Give the position of every malaria parasite and every leukocyte.
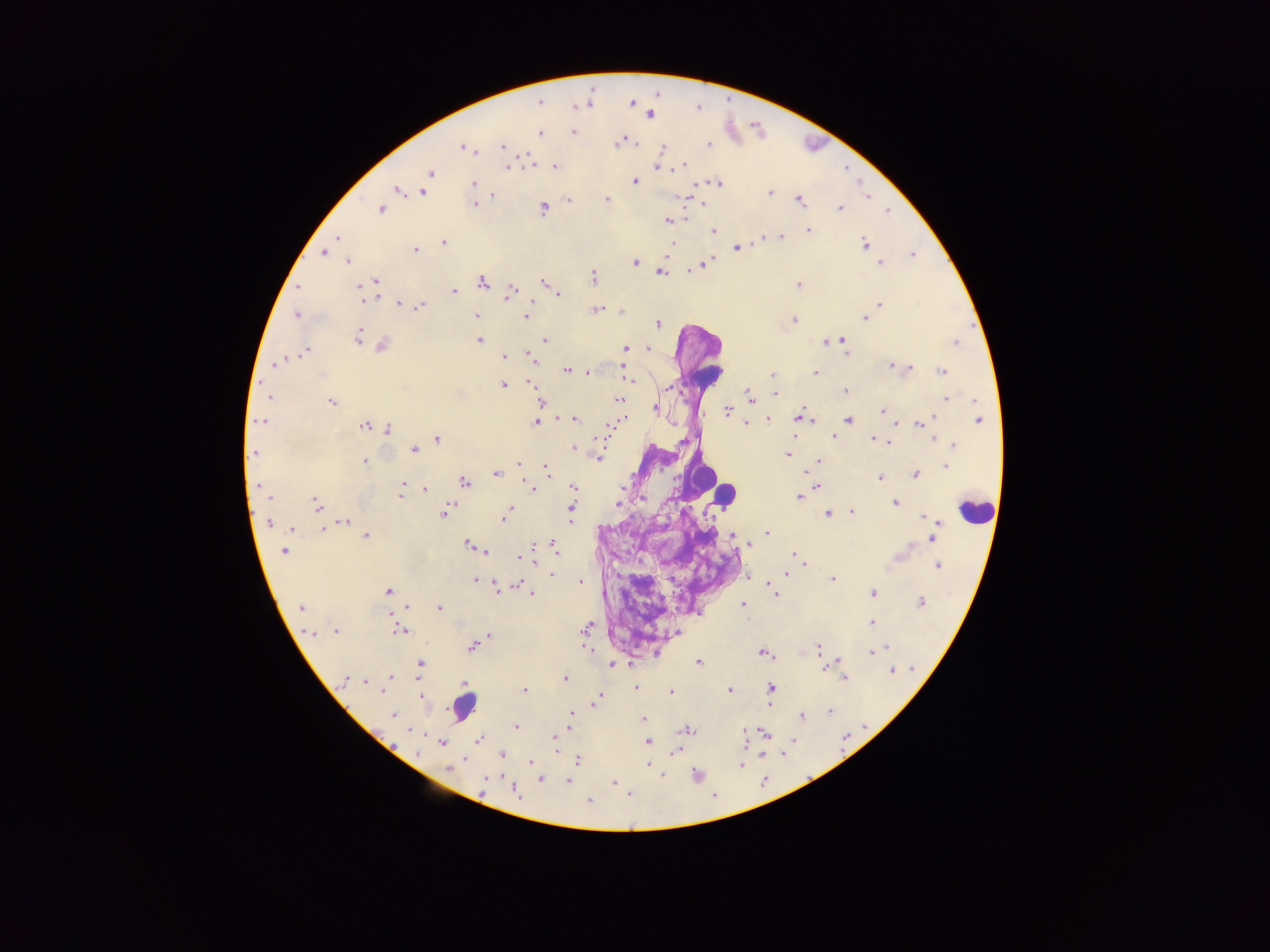

Approximate centers as {x, y} in pixels.
Malaria parasites: {540, 102}, {632, 103}, {589, 104}, {575, 105}, {650, 114}, {573, 132}, {539, 133}, {618, 142}, {503, 145}, {709, 145}, {464, 147}, {660, 148}, {528, 160}, {683, 164}, {507, 167}, {554, 167}, {659, 167}, {430, 173}, {635, 181}, {717, 182}, {473, 184}, {398, 189}, {423, 192}, {770, 193}, {491, 194}, {867, 196}, {681, 197}, {606, 199}, {799, 199}, {568, 201}, {702, 202}, {472, 203}, {542, 207}, {381, 208}, {840, 208}, {885, 211}, {668, 220}, {808, 231}, {713, 232}, {775, 236}, {781, 236}, {337, 238}, {762, 239}, {442, 242}, {865, 245}, {735, 248}, {414, 249}, {323, 253}, {912, 255}, {348, 260}, {635, 263}, {880, 263}, {703, 264}, {660, 271}, {592, 277}, {375, 281}, {482, 281}, {544, 283}, {798, 284}, {373, 285}, {298, 287}, {454, 291}, {509, 291}, {364, 292}, {376, 293}, {559, 295}, {532, 300}, {399, 303}, {879, 304}, {420, 306}, {597, 309}, {620, 311}, {297, 315}, {476, 315}, {526, 317}, {864, 318}, {793, 320}, {658, 324}, {358, 336}, {365, 340}, {479, 340}, {544, 340}, {841, 340}, {827, 342}, {956, 342}, {381, 345}, {625, 348}, {647, 348}, {304, 351}, {844, 351}, {528, 355}, {503, 356}, {278, 363}, {893, 365}, {903, 367}, {910, 368}, {567, 370}, {625, 370}, {587, 372}, {941, 372}, {815, 373}, {772, 375}, {531, 382}, {631, 382}, {503, 385}, {844, 391}, {775, 394}, {749, 396}, {268, 398}, {947, 399}, {618, 400}, {331, 402}, {540, 402}, {654, 409}, {726, 410}, {882, 411}, {799, 415}, {574, 418}, {767, 418}, {932, 418}, {979, 419}, {848, 420}, {812, 421}, {260, 422}, {535, 422}, {894, 423}, {917, 423}, {745, 424}, {364, 425}, {387, 430}, {833, 436}, {436, 438}, {874, 438}, {932, 439}, {889, 440}, {882, 441}, {954, 444}, {413, 449}, {574, 449}, {254, 452}, {786, 454}, {598, 457}, {365, 461}, {820, 461}, {518, 464}, {946, 465}, {546, 468}, {804, 472}, {496, 474}, {914, 474}, {880, 477}, {464, 482}, {525, 482}, {260, 486}, {403, 486}, {531, 486}, {572, 486}, {816, 486}, {622, 487}, {425, 489}, {265, 493}, {400, 493}, {798, 496}, {268, 497}, {641, 498}, {893, 502}, {316, 504}, {510, 507}, {571, 508}, {444, 511}, {852, 512}, {827, 513}, {924, 516}, {504, 518}, {930, 519}, {343, 521}, {935, 521}, {269, 523}, {290, 528}, {322, 528}, {766, 533}, {365, 535}, {731, 535}, {932, 537}, {746, 542}, {749, 544}, {468, 546}, {554, 546}, {284, 550}, {485, 550}, {793, 553}, {518, 557}, {938, 565}, {804, 566}, {550, 574}, {788, 574}, {748, 576}, {832, 579}, {475, 580}, {579, 582}, {517, 584}, {493, 585}, {768, 585}, {388, 591}, {532, 593}, {873, 593}, {776, 596}, {920, 601}, {742, 605}, {407, 607}, {439, 607}, {301, 608}, {391, 614}, {871, 623}, {586, 627}, {335, 630}, {400, 631}, {309, 632}, {676, 632}, {489, 637}, {471, 646}, {884, 647}, {586, 648}, {819, 649}, {870, 652}, {763, 653}, {698, 662}, {836, 662}, {419, 664}, {611, 665}, {823, 667}, {891, 670}, {389, 678}, {564, 678}, {844, 678}, {344, 680}, {365, 680}, {354, 682}, {463, 683}, {636, 687}, {771, 688}, {523, 690}, {729, 691}, {669, 692}, {598, 694}, {421, 697}, {595, 700}, {769, 703}, {829, 710}, {571, 714}, {801, 715}, {394, 716}, {644, 718}, {569, 721}, {515, 726}, {685, 729}, {743, 732}, {764, 732}, {477, 739}, {553, 740}, {646, 742}, {440, 743}, {556, 743}, {675, 751}, {502, 755}, {529, 762}, {576, 762}, {742, 763}, {646, 764}, {449, 767}, {485, 779}, {540, 779}, {568, 781}, {614, 783}, {514, 790}, {589, 800}.
Leukocytes: {706, 377}, {701, 475}, {726, 496}, {975, 510}, {464, 706}.

Sample from Ghana. Thick blood smear. One field of view. Image is 1270×952 pixels. Mobile-phone photograph taken through the microscope.